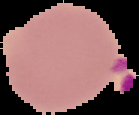

image type = segmented cell region with the area outside set to black
image size = 139×115 pixels
result = Plasmodium parasites identified
preparation = thin blood smear